Locate every blood parasite and identify its species.
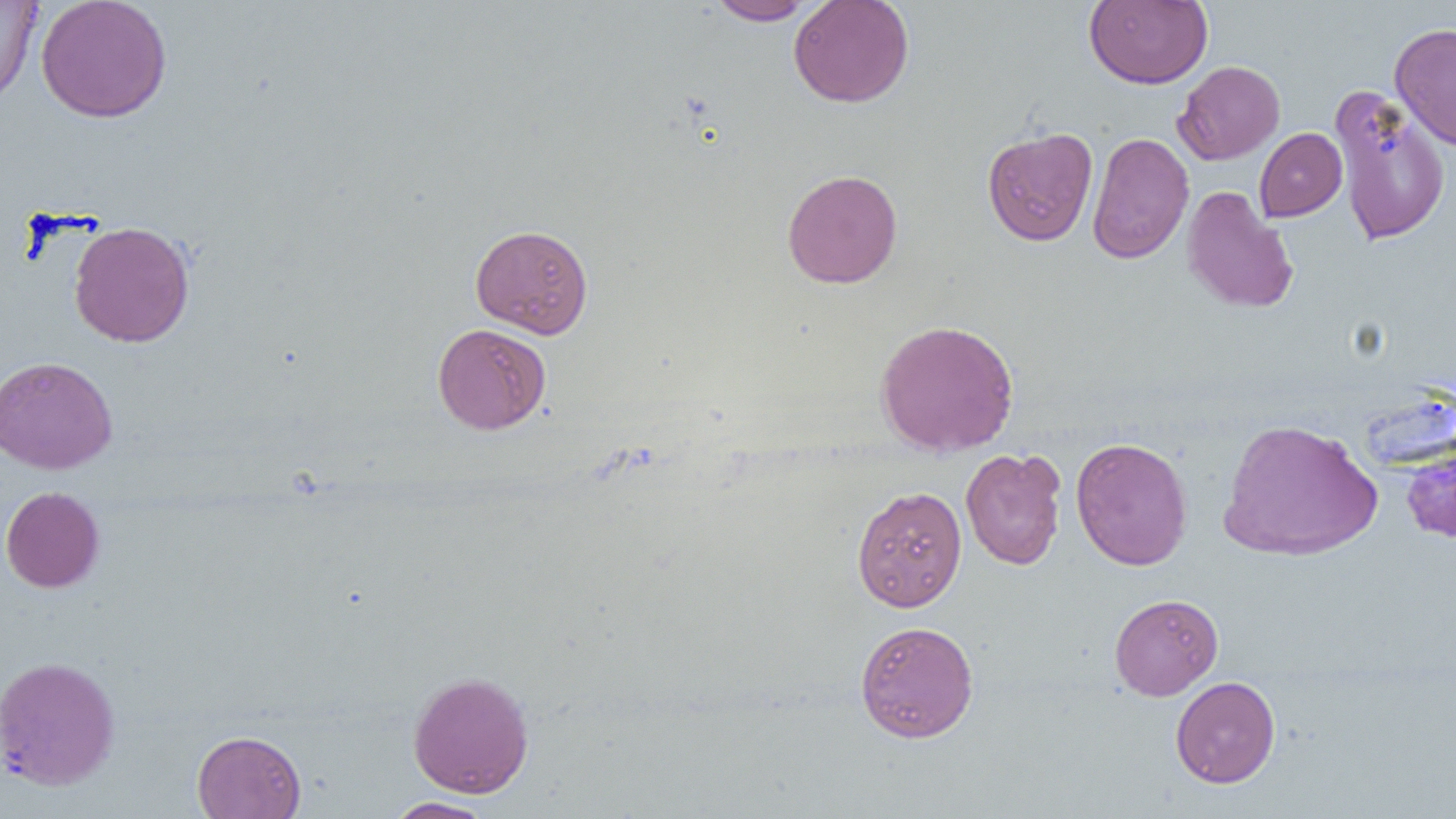

No blood parasites observed.

Summary:
  - Coordinate format: approximate bounding boxes as [x1, y1, x2, y2] in pixels
  - Uninfected red blood cell locations: [0, 0, 42, 108], [35, 0, 173, 123], [788, 0, 915, 108], [1084, 0, 1213, 88], [709, 1, 816, 25], [1390, 22, 1456, 151], [1173, 60, 1285, 164], [1329, 83, 1452, 246], [982, 126, 1098, 246], [1254, 127, 1347, 222], [1087, 132, 1193, 264], [781, 169, 903, 288], [1182, 186, 1298, 314], [68, 220, 195, 347], [470, 223, 594, 339], [875, 318, 1019, 457], [432, 322, 551, 434], [0, 356, 117, 474], [1217, 417, 1382, 561], [1070, 437, 1193, 571], [960, 447, 1066, 570], [1401, 448, 1456, 543], [851, 485, 967, 612], [1, 486, 104, 593], [1108, 593, 1223, 700], [854, 620, 979, 742], [0, 655, 121, 791], [407, 670, 535, 798], [1170, 676, 1280, 788], [192, 729, 306, 818], [385, 797, 497, 818]
  - Slide-level diagnosis: negative for blood parasites
  - Magnification: 1000x
  - Image size: 1456×819 pixels
  - Modality: optical microscopy
  - Preparation: thin blood film
  - Field of view: single